Which red blood cells are P. falciparum-infected, and which are of indeterminate infection status?
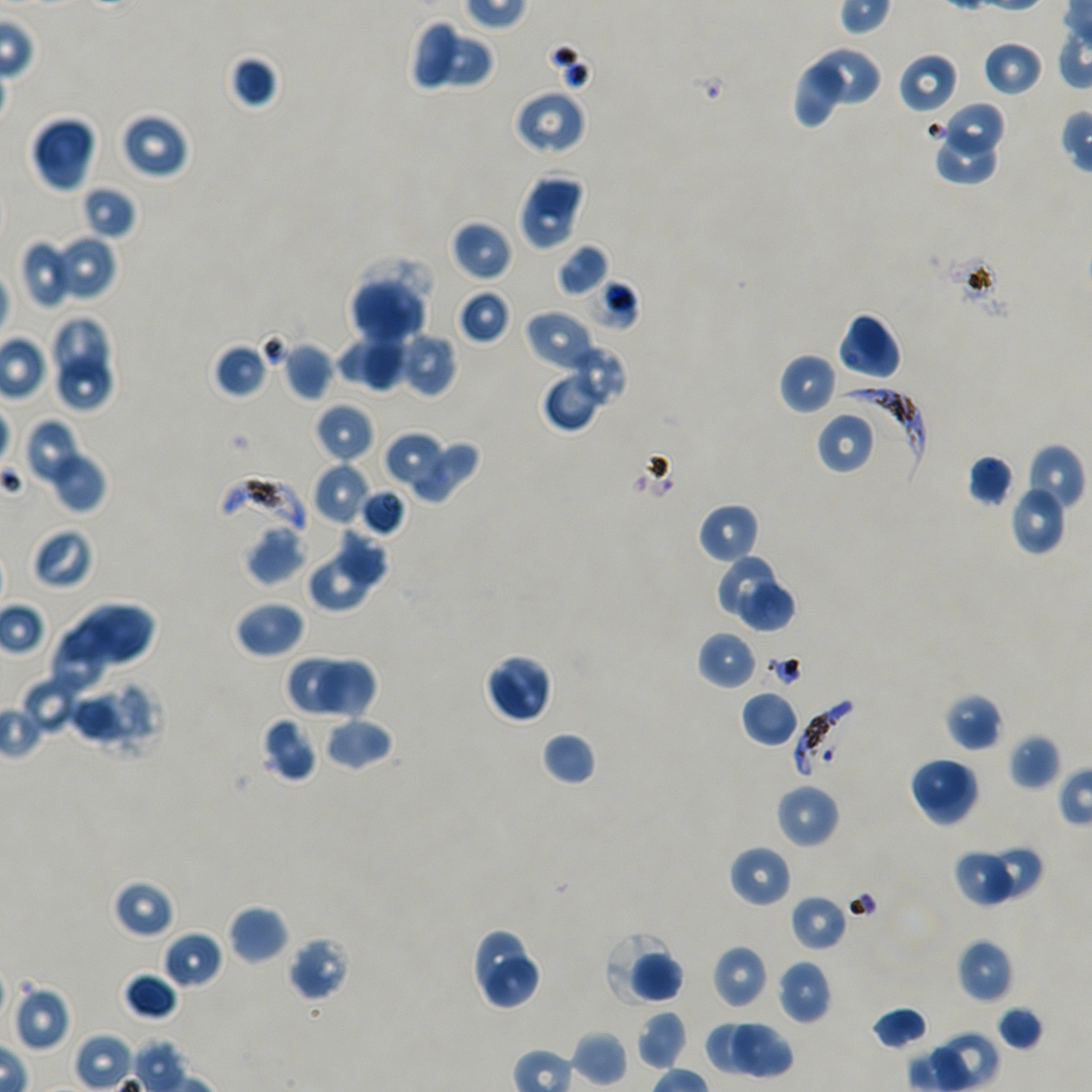
Approximate bounding boxes as {x1, y1, x2, y2} in pixels. Not every red blood cell is marked.
Infected red blood cells: {837, 386, 923, 480}, {218, 474, 307, 536}, {794, 697, 862, 777}.
Red blood cells of indeterminate infection status: {584, 278, 640, 332}.

Locations of uninfected red blood cells: {411, 20, 455, 88}, {425, 32, 495, 91}, {981, 39, 1044, 97}, {812, 48, 883, 106}, {226, 53, 280, 110}, {899, 53, 959, 114}, {793, 63, 849, 130}, {512, 88, 587, 156}, {943, 101, 1006, 156}, {120, 111, 189, 180}, {31, 115, 97, 192}, {930, 132, 1001, 185}, {518, 171, 586, 251}, {81, 185, 136, 241}, {450, 220, 511, 281}, {50, 235, 117, 302}, {18, 238, 76, 309}, {556, 243, 609, 297}, {350, 274, 429, 345}, {456, 289, 511, 345}, {524, 310, 597, 372}, {838, 313, 901, 382}, {54, 318, 110, 382}, {397, 331, 458, 399}, {362, 332, 403, 390}, {335, 335, 407, 393}, {279, 341, 335, 401}, {213, 342, 269, 399}, {574, 344, 626, 405}, {779, 352, 837, 414}, {58, 354, 113, 410}, {541, 367, 607, 431}, {314, 403, 375, 463}, {816, 410, 877, 475}, {22, 418, 91, 492}, {383, 431, 446, 492}, {411, 437, 479, 504}, {1023, 443, 1086, 516}, {45, 447, 107, 514}, {966, 453, 1015, 507}, {312, 462, 369, 526}, {1008, 484, 1068, 556}, {358, 487, 407, 536}, {697, 503, 761, 565}, {337, 520, 392, 590}, {245, 526, 307, 585}, {32, 527, 94, 590}, {714, 553, 777, 615}, {306, 554, 371, 612}, {739, 579, 799, 636}, {234, 599, 306, 659}, {55, 601, 155, 674}, {47, 624, 106, 695}, {697, 631, 757, 690}, {484, 654, 553, 724}, {285, 655, 349, 714}, {318, 659, 380, 722}, {20, 674, 87, 734}, {94, 682, 158, 752}, {740, 691, 800, 748}, {943, 692, 1004, 752}, {70, 695, 141, 747}, {261, 716, 316, 782}, {323, 716, 394, 771}, {541, 731, 597, 786}, {1008, 733, 1062, 790}, {909, 756, 971, 812}, {924, 766, 981, 825}, {775, 783, 839, 849}, {728, 845, 792, 908}, {982, 848, 1044, 900}, {953, 852, 1014, 907}, {111, 878, 176, 939}, {789, 893, 848, 953}, {227, 905, 289, 964}, {162, 929, 223, 989}, {475, 930, 526, 998}, {604, 933, 684, 1008}, {287, 936, 352, 1002}, {956, 938, 1014, 1003}, {712, 944, 768, 1009}, {486, 954, 541, 1008}, {776, 960, 833, 1024}, {123, 971, 179, 1021}, {12, 984, 71, 1051}, {996, 1004, 1044, 1051}, {871, 1006, 928, 1051}, {636, 1010, 687, 1071}, {706, 1019, 766, 1074}, {731, 1022, 794, 1078}, {570, 1029, 629, 1089}. 100x oil-immersion objective, numerical aperture 1.45. Single field of view. Giemsa-stained preparation. P. falciparum strain NF54 maintained in static in-vitro culture. Thin blood film. Image is 1092×1092 pixels. Donor blood group A+/O+.